Name the blood parasite species.
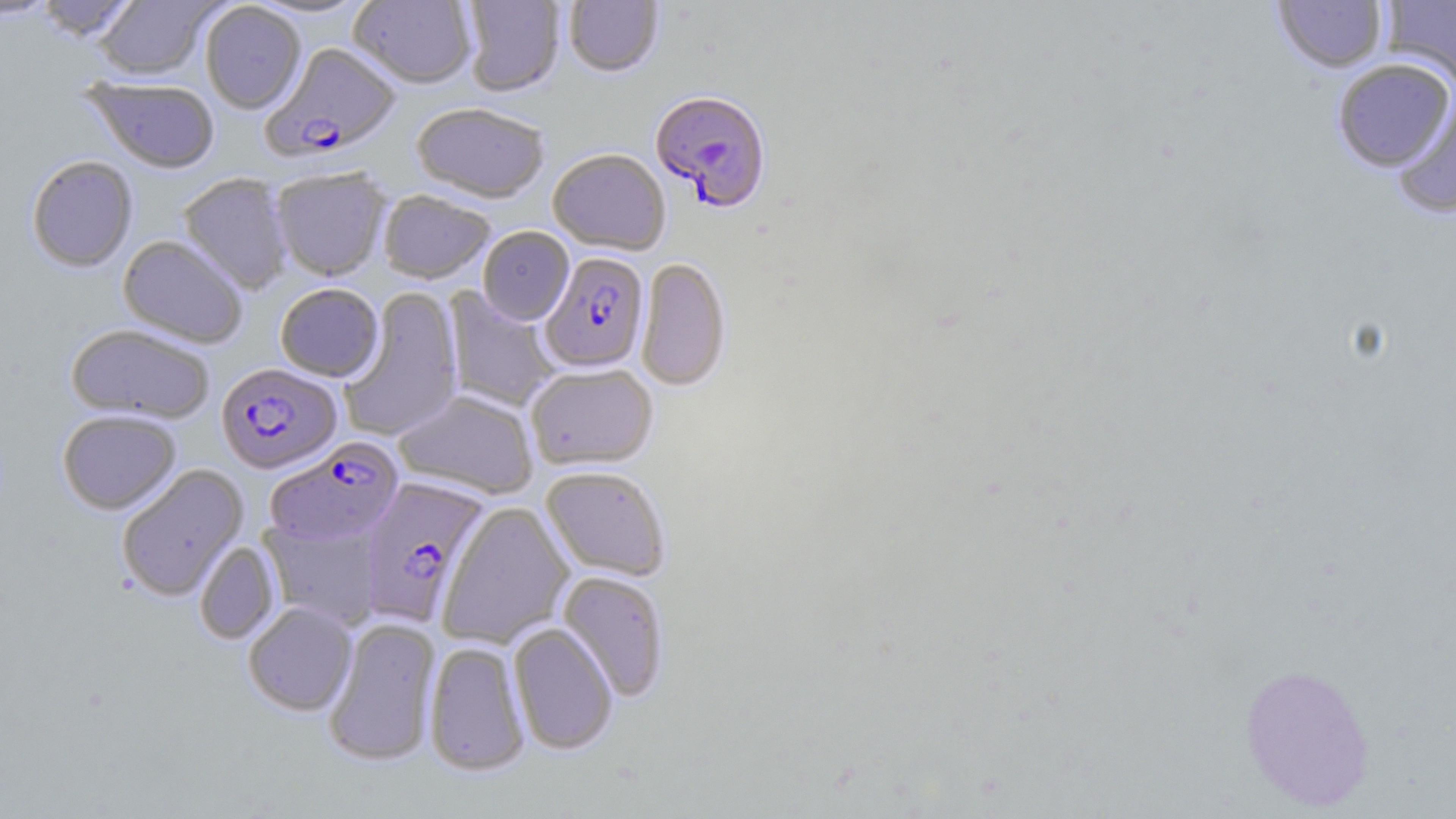

Plasmodium falciparum.

Summary:
  - Coordinate format: approximate bounding boxes as [x1, y1, x2, y2] in pixels
  - Plasmodium falciparum-infected red blood cell locations: [259, 44, 400, 164], [650, 93, 772, 215], [540, 253, 649, 375], [216, 364, 343, 475], [265, 439, 403, 547], [358, 477, 490, 627]
  - Uninfected red blood cell locations: [0, 0, 58, 20], [36, 0, 138, 42], [94, 0, 220, 82], [244, 0, 374, 21], [349, 0, 476, 90], [462, 0, 565, 98], [564, 0, 663, 79], [1381, 0, 1456, 87], [1272, 1, 1387, 73], [200, 2, 306, 115], [1332, 58, 1455, 172], [84, 79, 220, 175], [1391, 86, 1456, 218], [411, 105, 549, 206], [548, 151, 670, 256], [26, 156, 138, 273], [271, 169, 391, 283], [177, 174, 293, 295], [378, 192, 495, 286], [478, 228, 574, 326], [118, 236, 247, 349], [636, 258, 731, 392], [275, 284, 384, 383], [339, 287, 464, 442], [443, 287, 560, 412], [65, 324, 214, 425], [526, 365, 658, 471], [394, 390, 538, 499], [57, 411, 181, 515], [116, 464, 249, 602], [541, 467, 670, 582], [437, 502, 576, 648], [259, 517, 384, 630], [194, 541, 280, 645], [556, 571, 670, 703], [243, 602, 358, 716], [322, 617, 440, 767], [508, 623, 618, 756], [424, 642, 531, 777], [1238, 663, 1376, 811]
  - Modality: optical microscopy
  - Stain: May-Grünwald-Giemsa
  - Preparation: thin blood smear
  - Image size: 1456×819 pixels
  - Magnification: 1000x
  - Field of view: one of a larger specimen